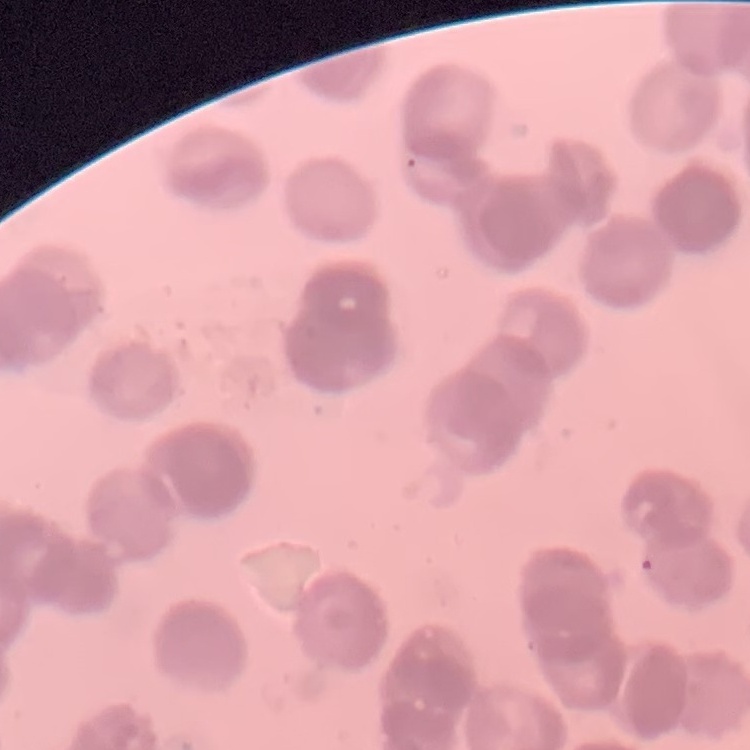
erythrocyte morphology = rouleaux formation
preparation = thin blood film
stain = Field's or Giemsa
image type = one tile cut from a larger photomicrograph